Identify the preparation type.
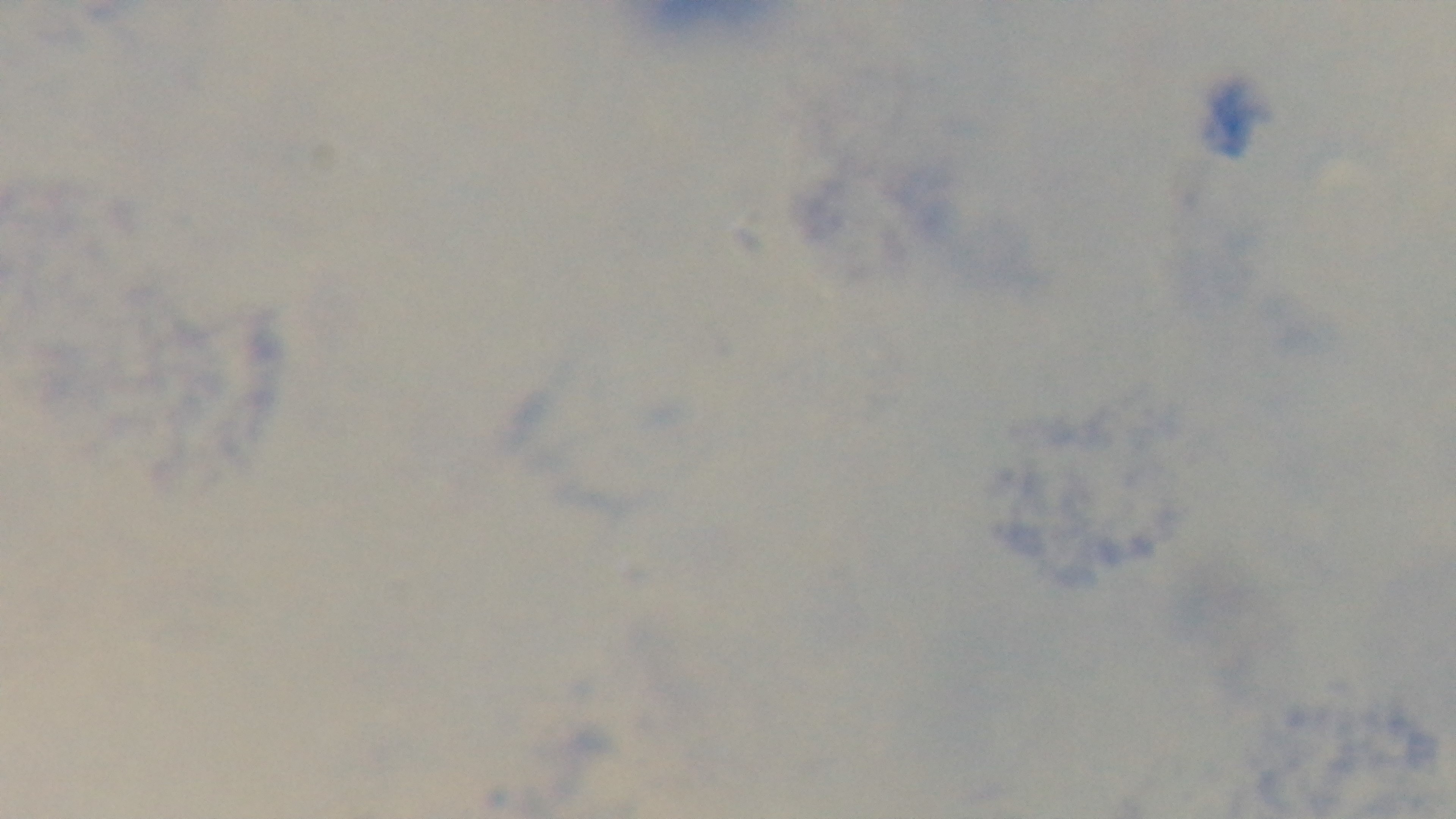

A thick smear.

objective: 100x oil immersion
capture: mounted 4K digital camera
malaria_status: uninfected
field_of_view: single
stain: Giemsa
modality: light microscopy